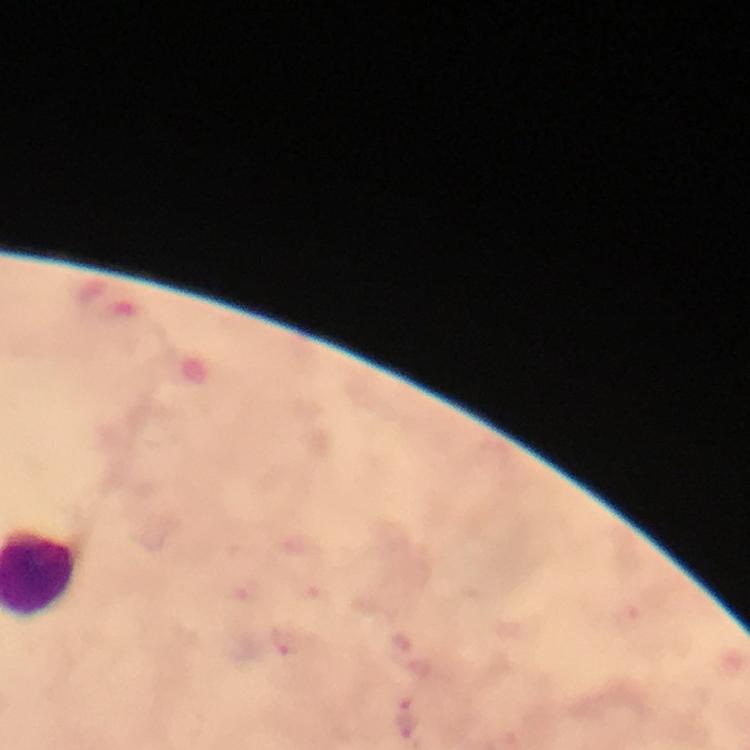
Approximate centers as {x, y} in pixels.
Summary:
  - Malaria parasite locations: {288, 640}, {412, 718}
  - Capture: smartphone camera through the microscope
  - Context: from a malaria diagnostic workup
  - Image size: 750×750 pixels
  - Cropped from: a single field of view
  - Immersion oil: used
  - Preparation: thick blood smear
  - Magnification: 100x
  - Stain: Giemsa